Identify the parasite.
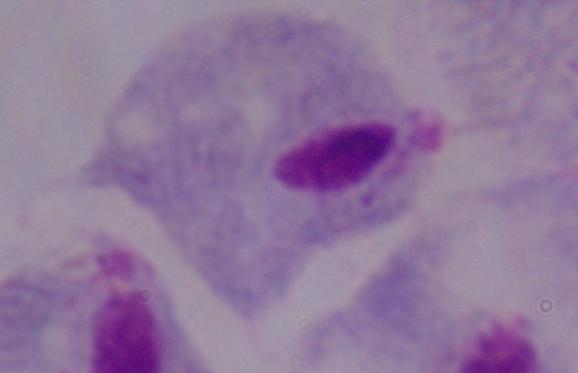

A trichomonad.

1000x magnification. Micrograph.